State which parasite is depicted.
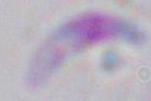
This is Toxoplasma gondii.

magnification = 1000x
modality = micrograph